State which cell type is depicted.
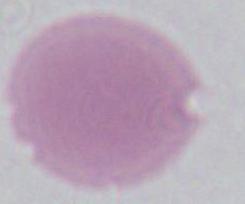

This is an erythrocyte.

magnification: 1000x
modality: photomicrograph